Assess the morphology of the red blood cells.
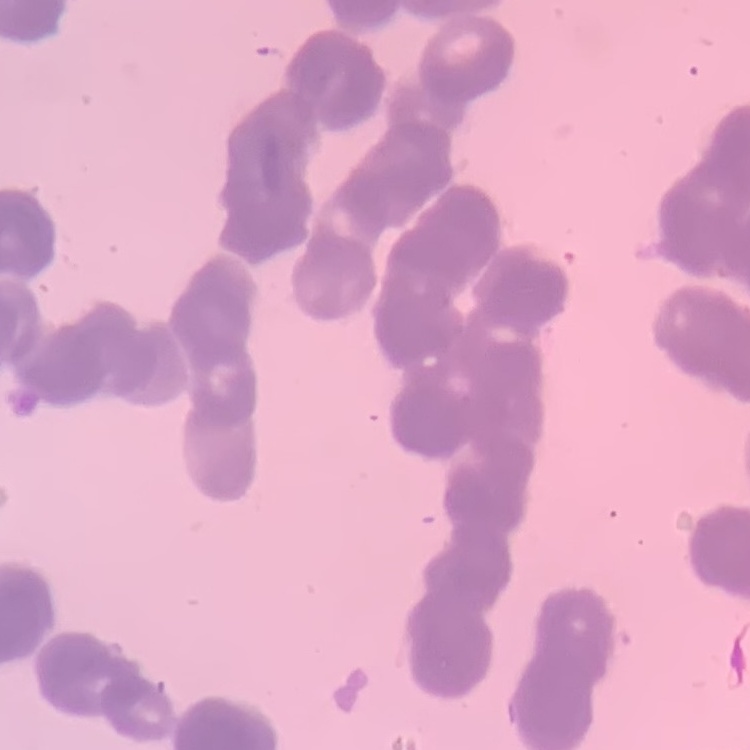

They show rouleaux formation.

{
  "image_type": "square crop of a larger photomicrograph",
  "stain": "Field's or Giemsa",
  "preparation": "thin peripheral smear"
}